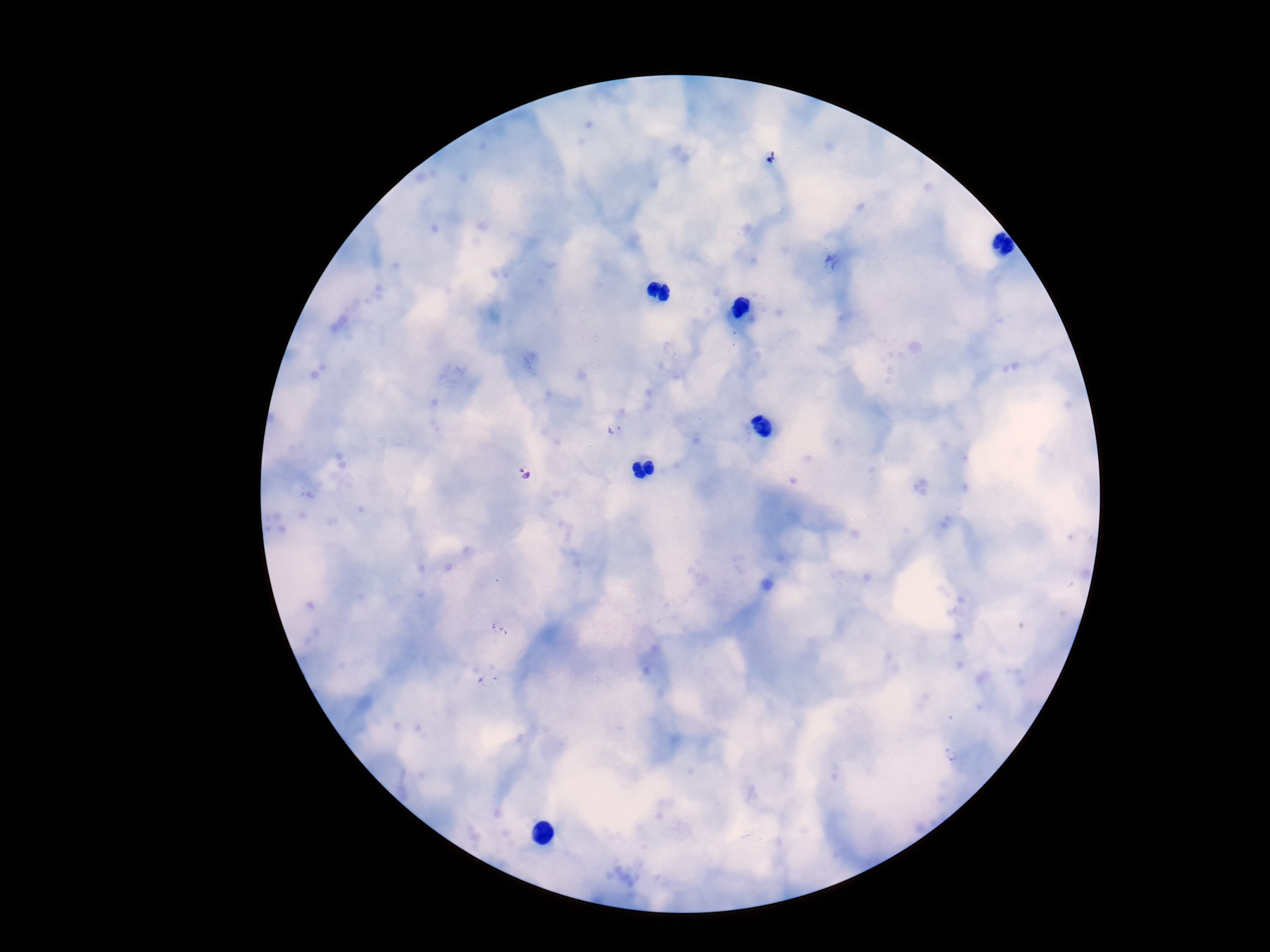
plasmodium_parasite_locations: 'approximate centers as [x, y] in pixels: [833, 262], [614, 428], [524, 473], [951, 754]'
magnification: 100x
stain: Giemsa
patient_malaria_status: infected
preparation: thick peripheral-blood smear
field_of_view: single
capture: smartphone camera through the microscope eyepiece
image_size: 1270×952 pixels